Assess this cell for malaria.
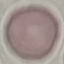

Uninfected.

Thin blood film. Cell patch, automatically extracted from a larger field of view and resized to 64 × 64 pixels. Photographed with a smartphone camera at the microscope eyepiece. Giemsa-stained preparation.